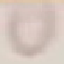
Summary:
  - Malaria status: uninfected
  - Image type: automatically extracted cell patch, resized to 64 × 64 pixels
  - Capture: smartphone through the microscope eyepiece
  - Stain: Giemsa
  - Preparation: thin blood film